Classify this cell by malaria status.
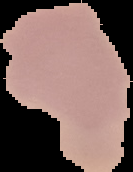

Uninfected.

Image is 133×172 pixels. From a thin blood film. Cell region segmented out of the field of view; the surrounding area is masked to black.